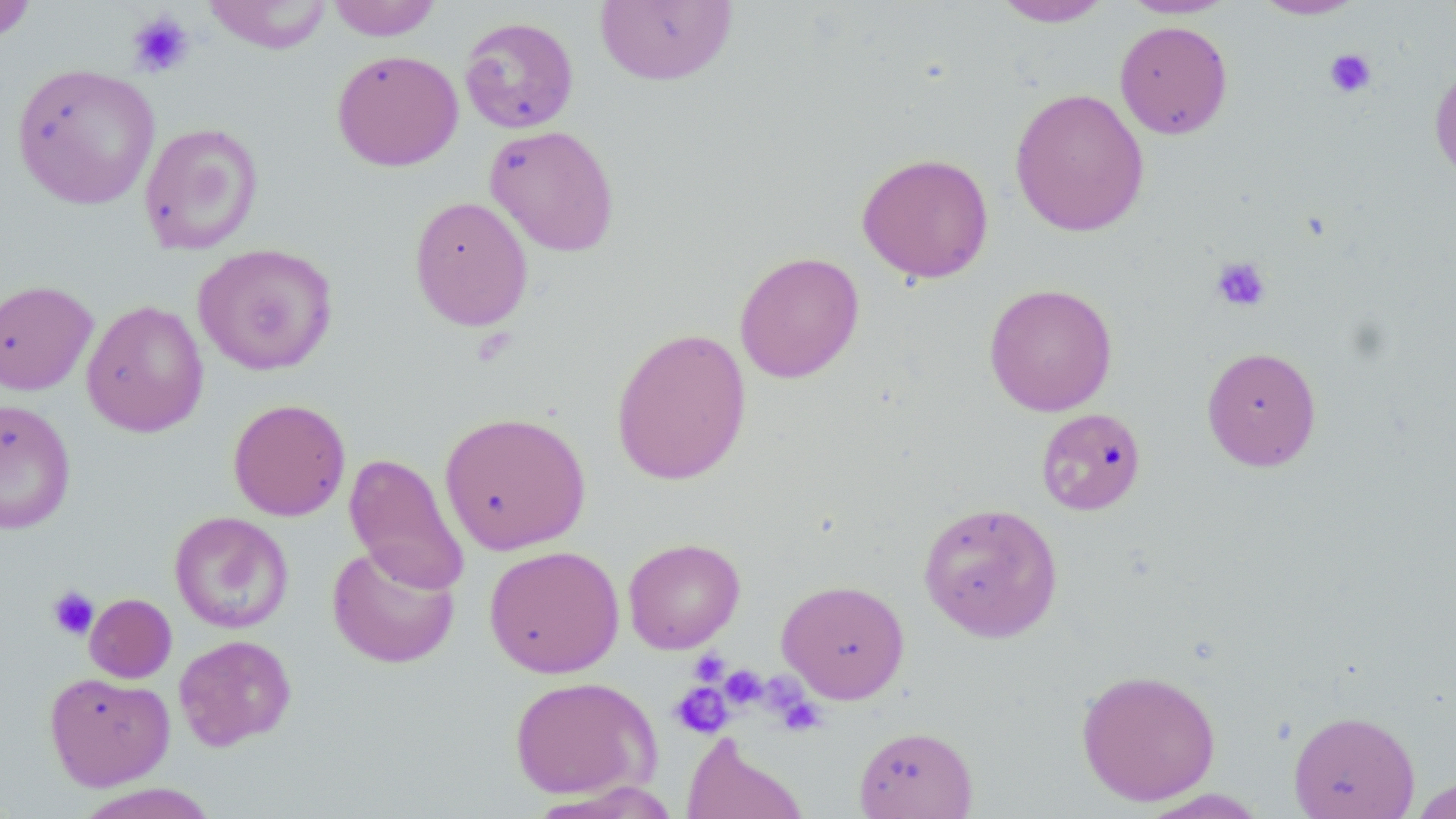

Summary:
  - Coordinate format: approximate bounding boxes as named x1/y1/x2/y2 corners in pixels
  - Platelet locations: (x1=127, y1=11, x2=195, y2=78), (x1=1324, y1=48, x2=1376, y2=98), (x1=1210, y1=256, x2=1271, y2=312), (x1=46, y1=585, x2=100, y2=640), (x1=689, y1=649, x2=729, y2=686), (x1=720, y1=665, x2=767, y2=708), (x1=670, y1=682, x2=732, y2=738), (x1=773, y1=691, x2=826, y2=735)
  - Uninfected red blood cell locations: (x1=203, y1=0, x2=333, y2=54), (x1=325, y1=0, x2=442, y2=41), (x1=595, y1=0, x2=738, y2=86), (x1=992, y1=0, x2=1114, y2=27), (x1=1119, y1=0, x2=1238, y2=18), (x1=1250, y1=0, x2=1367, y2=20), (x1=0, y1=1, x2=39, y2=42), (x1=459, y1=16, x2=579, y2=133), (x1=1114, y1=20, x2=1233, y2=139), (x1=331, y1=50, x2=464, y2=171), (x1=1429, y1=60, x2=1456, y2=186), (x1=11, y1=63, x2=161, y2=210), (x1=1009, y1=87, x2=1149, y2=237), (x1=139, y1=122, x2=264, y2=255), (x1=484, y1=124, x2=620, y2=257), (x1=856, y1=152, x2=994, y2=283), (x1=408, y1=195, x2=533, y2=331), (x1=192, y1=242, x2=339, y2=375), (x1=733, y1=251, x2=865, y2=383), (x1=0, y1=279, x2=99, y2=395), (x1=983, y1=282, x2=1119, y2=417), (x1=81, y1=300, x2=209, y2=437), (x1=611, y1=326, x2=751, y2=486), (x1=1201, y1=346, x2=1322, y2=471), (x1=228, y1=398, x2=351, y2=521), (x1=0, y1=399, x2=76, y2=535), (x1=1035, y1=407, x2=1147, y2=516), (x1=438, y1=411, x2=591, y2=555), (x1=344, y1=453, x2=470, y2=594), (x1=918, y1=501, x2=1063, y2=642), (x1=169, y1=511, x2=294, y2=634), (x1=623, y1=537, x2=745, y2=654), (x1=327, y1=542, x2=460, y2=669), (x1=484, y1=545, x2=624, y2=679), (x1=776, y1=579, x2=910, y2=703), (x1=84, y1=593, x2=177, y2=683), (x1=174, y1=634, x2=296, y2=750), (x1=1075, y1=668, x2=1221, y2=805), (x1=44, y1=671, x2=174, y2=791), (x1=509, y1=675, x2=660, y2=800), (x1=1288, y1=710, x2=1419, y2=819), (x1=854, y1=725, x2=979, y2=819), (x1=681, y1=733, x2=808, y2=819), (x1=1407, y1=776, x2=1456, y2=817), (x1=70, y1=783, x2=222, y2=819), (x1=1139, y1=789, x2=1268, y2=818)
  - Slide-level diagnosis: negative for blood parasites
  - Magnification: 1000x
  - Stain: May-Grünwald-Giemsa
  - Preparation: thin blood smear
  - Field of view: one of a larger specimen
  - Image size: 1456×819 pixels
  - Modality: light microscopy